Locate every blood parasite and identify its species.
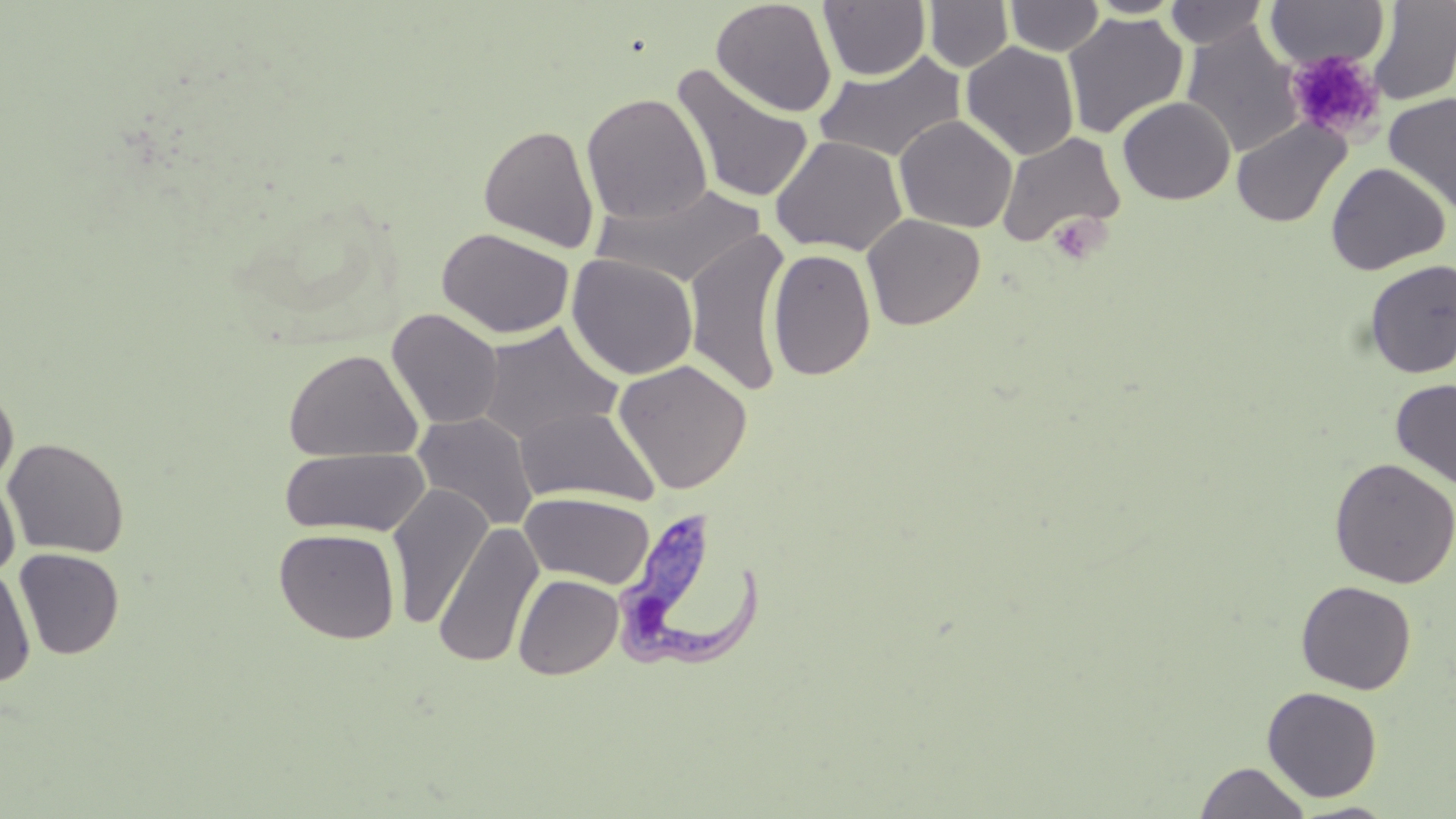
Approximate bounding boxes as named x1/y1/x2/y2 corners in pixels.
Trypanosoma brucei: (x1=614, y1=507, x2=770, y2=676).
No Plasmodium falciparum, Plasmodium ovale, Plasmodium malariae, Plasmodium vivax, or Babesia divergens observed.

Summary:
  - Platelet locations: (x1=1286, y1=50, x2=1385, y2=143), (x1=1047, y1=213, x2=1106, y2=266)
  - Uninfected red blood cell locations: (x1=711, y1=0, x2=837, y2=117), (x1=819, y1=0, x2=931, y2=81), (x1=924, y1=0, x2=1014, y2=72), (x1=1005, y1=0, x2=1105, y2=56), (x1=1086, y1=0, x2=1187, y2=18), (x1=1368, y1=0, x2=1456, y2=105), (x1=1165, y1=1, x2=1269, y2=49), (x1=1265, y1=1, x2=1389, y2=70), (x1=933, y1=7, x2=1042, y2=110), (x1=1063, y1=12, x2=1188, y2=139), (x1=1181, y1=23, x2=1304, y2=157), (x1=961, y1=42, x2=1079, y2=161), (x1=813, y1=51, x2=968, y2=163), (x1=671, y1=64, x2=815, y2=204), (x1=581, y1=92, x2=713, y2=226), (x1=1383, y1=92, x2=1456, y2=215), (x1=1117, y1=96, x2=1235, y2=204), (x1=894, y1=115, x2=1017, y2=233), (x1=1231, y1=118, x2=1351, y2=228), (x1=478, y1=124, x2=599, y2=253), (x1=996, y1=131, x2=1125, y2=249), (x1=770, y1=135, x2=907, y2=256), (x1=1326, y1=162, x2=1450, y2=274), (x1=591, y1=182, x2=768, y2=288), (x1=862, y1=213, x2=985, y2=330), (x1=436, y1=227, x2=575, y2=339), (x1=684, y1=230, x2=791, y2=396), (x1=767, y1=248, x2=876, y2=381), (x1=567, y1=254, x2=698, y2=380), (x1=1363, y1=259, x2=1456, y2=379), (x1=387, y1=308, x2=504, y2=430), (x1=477, y1=322, x2=623, y2=444), (x1=283, y1=349, x2=423, y2=463), (x1=613, y1=359, x2=753, y2=495), (x1=1391, y1=378, x2=1456, y2=489), (x1=0, y1=385, x2=18, y2=491), (x1=515, y1=405, x2=659, y2=507), (x1=412, y1=412, x2=538, y2=531), (x1=3, y1=438, x2=130, y2=558), (x1=278, y1=447, x2=431, y2=538), (x1=1329, y1=457, x2=1456, y2=589), (x1=0, y1=476, x2=20, y2=578), (x1=387, y1=483, x2=493, y2=629), (x1=520, y1=492, x2=655, y2=589), (x1=433, y1=521, x2=543, y2=668), (x1=274, y1=528, x2=400, y2=644), (x1=14, y1=548, x2=125, y2=659), (x1=1, y1=565, x2=36, y2=688), (x1=513, y1=574, x2=623, y2=679), (x1=1295, y1=580, x2=1417, y2=694), (x1=1262, y1=686, x2=1383, y2=801), (x1=1194, y1=761, x2=1312, y2=819), (x1=1289, y1=801, x2=1402, y2=818)
  - Slide-level diagnosis: Trypanosoma brucei
  - Modality: light microscopy
  - Magnification: 1000x
  - Stain: May-Grünwald-Giemsa
  - Preparation: thin blood smear
  - Field of view: single
  - Image size: 1456×819 pixels